Report the malaria status of this cell.
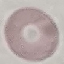

It is uninfected.

Summary:
  - Preparation: thin blood film
  - Stain: Giemsa
  - Capture: smartphone camera at the microscope eyepiece
  - Image type: cell patch, automatically extracted from a larger field of view and resized to 64 × 64 pixels